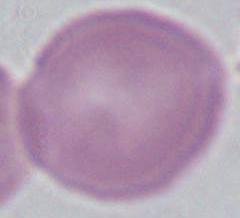

Summary:
  - Modality: photomicrograph
  - Identification: erythrocyte
  - Magnification: 1000x